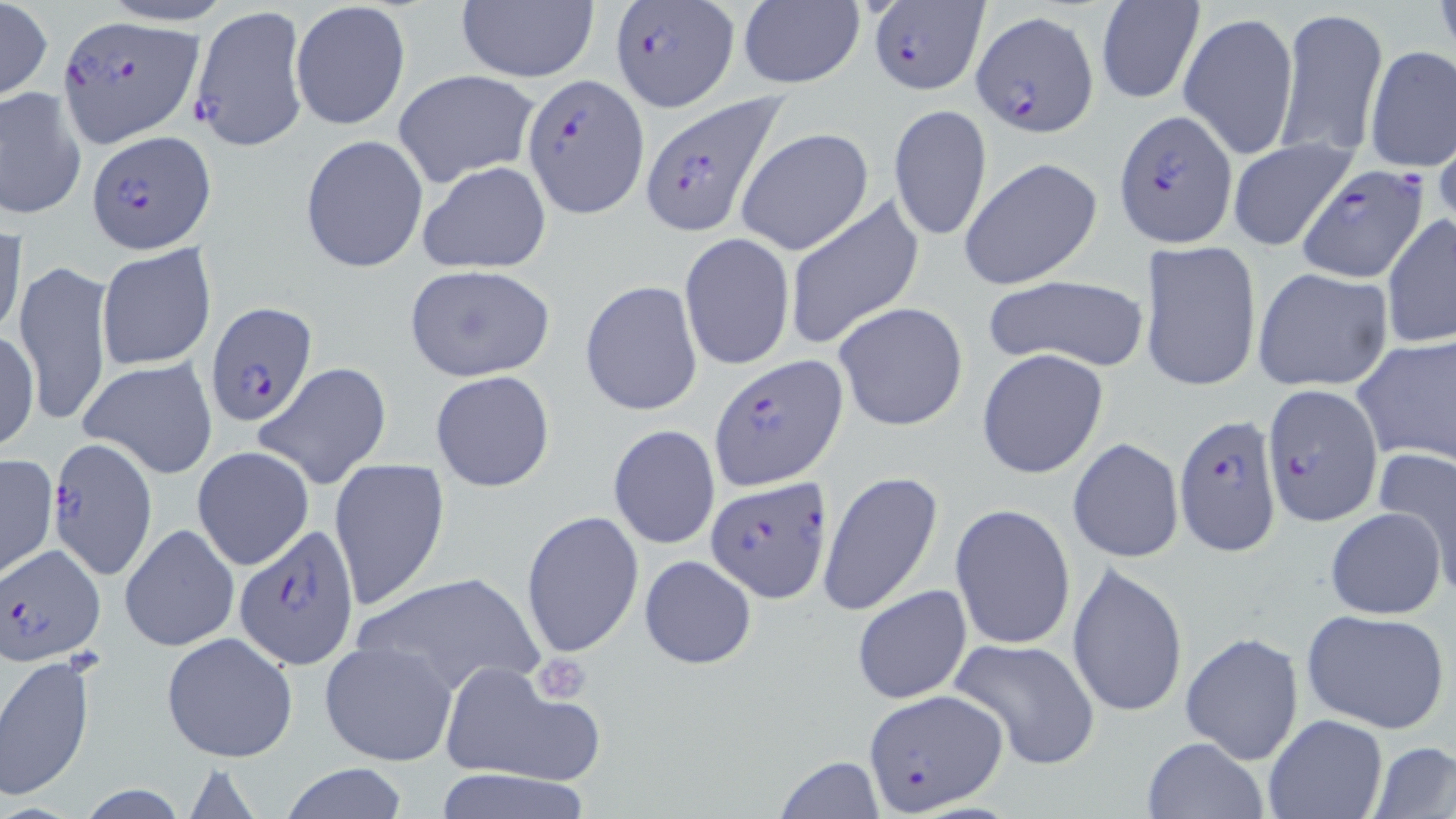
Approximate bounding boxes as named x1/y1/x2/y2 corners in pixels. Uninfected red blood cell locations: (x1=94, y1=0, x2=241, y2=26), (x1=1432, y1=0, x2=1456, y2=67), (x1=0, y1=1, x2=52, y2=101), (x1=292, y1=1, x2=411, y2=129), (x1=455, y1=1, x2=600, y2=84), (x1=1094, y1=1, x2=1205, y2=104), (x1=737, y1=2, x2=868, y2=90), (x1=1277, y1=5, x2=1386, y2=161), (x1=1179, y1=8, x2=1299, y2=162), (x1=1364, y1=45, x2=1456, y2=176), (x1=394, y1=69, x2=540, y2=187), (x1=1, y1=87, x2=86, y2=220), (x1=887, y1=104, x2=994, y2=242), (x1=734, y1=127, x2=875, y2=256), (x1=299, y1=134, x2=428, y2=272), (x1=1228, y1=138, x2=1356, y2=251), (x1=958, y1=157, x2=1103, y2=291), (x1=416, y1=161, x2=552, y2=274), (x1=782, y1=195, x2=925, y2=351), (x1=1382, y1=213, x2=1456, y2=349), (x1=0, y1=226, x2=26, y2=340), (x1=679, y1=232, x2=795, y2=371), (x1=1139, y1=238, x2=1262, y2=392), (x1=96, y1=243, x2=217, y2=371), (x1=13, y1=259, x2=113, y2=430), (x1=402, y1=263, x2=556, y2=383), (x1=1251, y1=267, x2=1394, y2=391), (x1=982, y1=273, x2=1151, y2=373), (x1=579, y1=280, x2=704, y2=417), (x1=833, y1=301, x2=968, y2=431), (x1=1, y1=327, x2=38, y2=454), (x1=1351, y1=334, x2=1456, y2=467), (x1=977, y1=348, x2=1109, y2=479), (x1=81, y1=356, x2=218, y2=478), (x1=252, y1=362, x2=393, y2=491), (x1=431, y1=371, x2=555, y2=492), (x1=608, y1=423, x2=720, y2=550), (x1=1068, y1=438, x2=1183, y2=564), (x1=192, y1=446, x2=315, y2=571), (x1=1374, y1=446, x2=1456, y2=586), (x1=0, y1=454, x2=57, y2=580), (x1=329, y1=459, x2=450, y2=614), (x1=818, y1=469, x2=945, y2=618), (x1=950, y1=503, x2=1076, y2=652), (x1=1326, y1=506, x2=1447, y2=619), (x1=520, y1=509, x2=644, y2=660), (x1=120, y1=522, x2=239, y2=651), (x1=639, y1=555, x2=757, y2=670), (x1=1066, y1=560, x2=1189, y2=719), (x1=352, y1=569, x2=546, y2=699), (x1=852, y1=584, x2=972, y2=705), (x1=1301, y1=608, x2=1451, y2=735), (x1=161, y1=632, x2=298, y2=762), (x1=1180, y1=632, x2=1304, y2=765), (x1=948, y1=635, x2=1102, y2=772), (x1=320, y1=640, x2=459, y2=766), (x1=0, y1=653, x2=98, y2=801), (x1=439, y1=662, x2=602, y2=786), (x1=1263, y1=714, x2=1386, y2=819), (x1=1140, y1=737, x2=1271, y2=819), (x1=1369, y1=740, x2=1456, y2=818), (x1=775, y1=756, x2=885, y2=818), (x1=279, y1=762, x2=410, y2=819), (x1=431, y1=768, x2=599, y2=819). Platelet locations: (x1=530, y1=653, x2=591, y2=705). Plasmodium falciparum-infected red blood cell locations: (x1=610, y1=0, x2=739, y2=111), (x1=870, y1=1, x2=985, y2=94), (x1=189, y1=5, x2=308, y2=152), (x1=972, y1=8, x2=1098, y2=137), (x1=61, y1=17, x2=203, y2=145), (x1=522, y1=72, x2=647, y2=217), (x1=641, y1=94, x2=789, y2=234), (x1=1113, y1=110, x2=1237, y2=247), (x1=87, y1=131, x2=215, y2=255), (x1=1297, y1=163, x2=1427, y2=282), (x1=205, y1=302, x2=318, y2=427), (x1=709, y1=355, x2=847, y2=490), (x1=1259, y1=382, x2=1385, y2=527), (x1=1173, y1=415, x2=1283, y2=555), (x1=46, y1=441, x2=155, y2=581), (x1=705, y1=476, x2=834, y2=602), (x1=231, y1=526, x2=356, y2=667), (x1=1, y1=545, x2=104, y2=666), (x1=866, y1=689, x2=1005, y2=814). Slide-level diagnosis: Plasmodium falciparum. Captured at 1000x magnification. Light microscopy. Thin blood smear. May-Grünwald-Giemsa stain. One field of a larger specimen. Image is 1456×819 pixels.